Assess the morphology of the red blood cells.
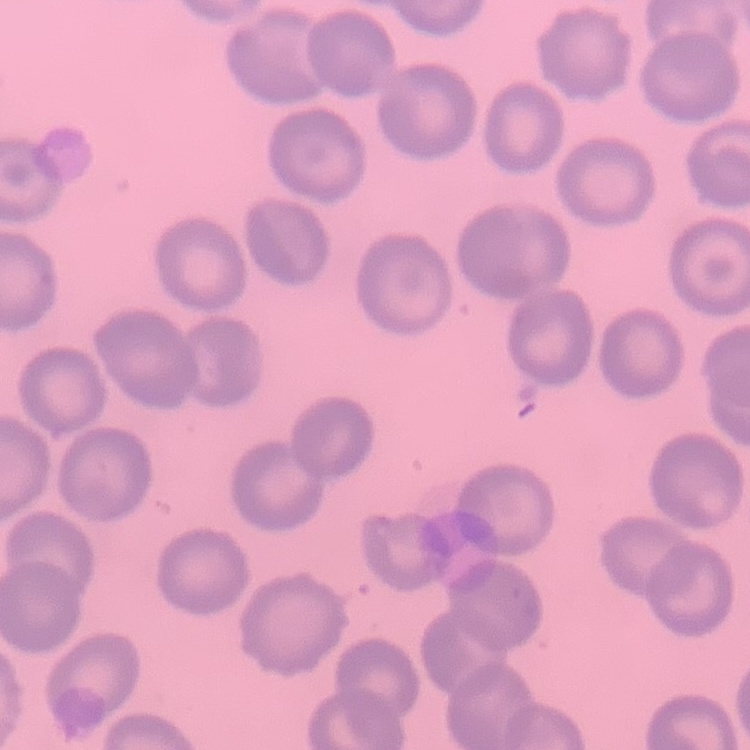
No rouleaux formation.

image_type: one tile cut from a larger photomicrograph
preparation: thin blood film
stain: Field's or Giemsa